Identify the parasite.
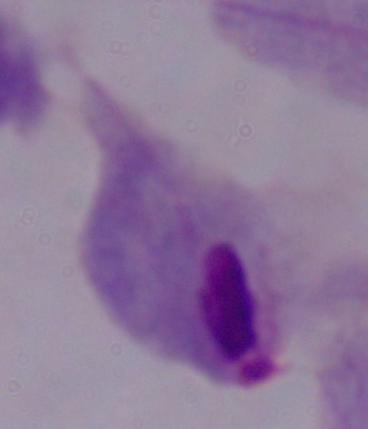
A trichomonad.

1000x magnification. Photomicrograph.